Report the malaria status of this cell.
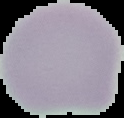

Uninfected.

Summary:
  - Image type: segmented cell region on a black background
  - Image size: 124×118 pixels
  - Preparation: thin blood film